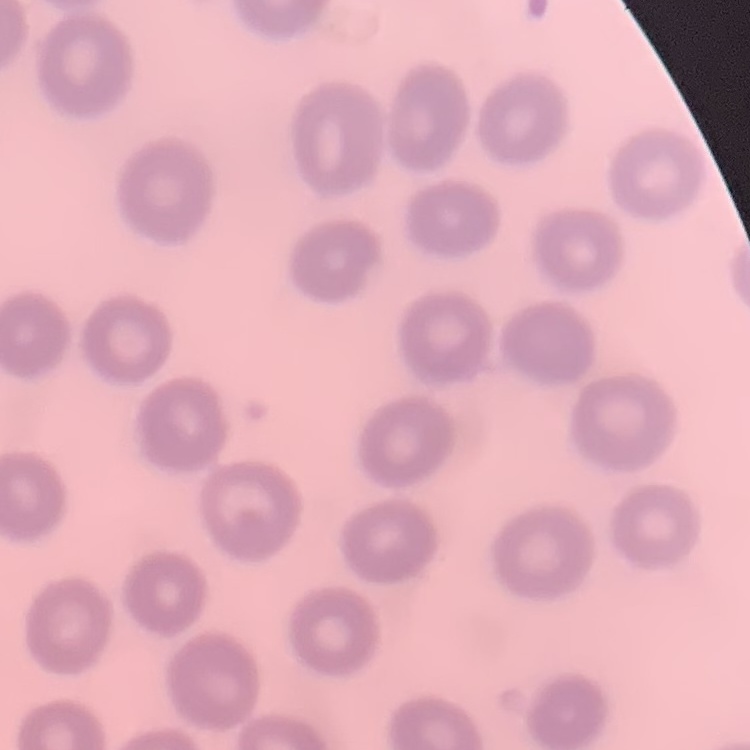

red blood cell morphology = no rouleaux formation
image type = square crop of a larger photomicrograph
preparation = thin peripheral smear
stain = Field's or Giemsa